Assess for malaria.
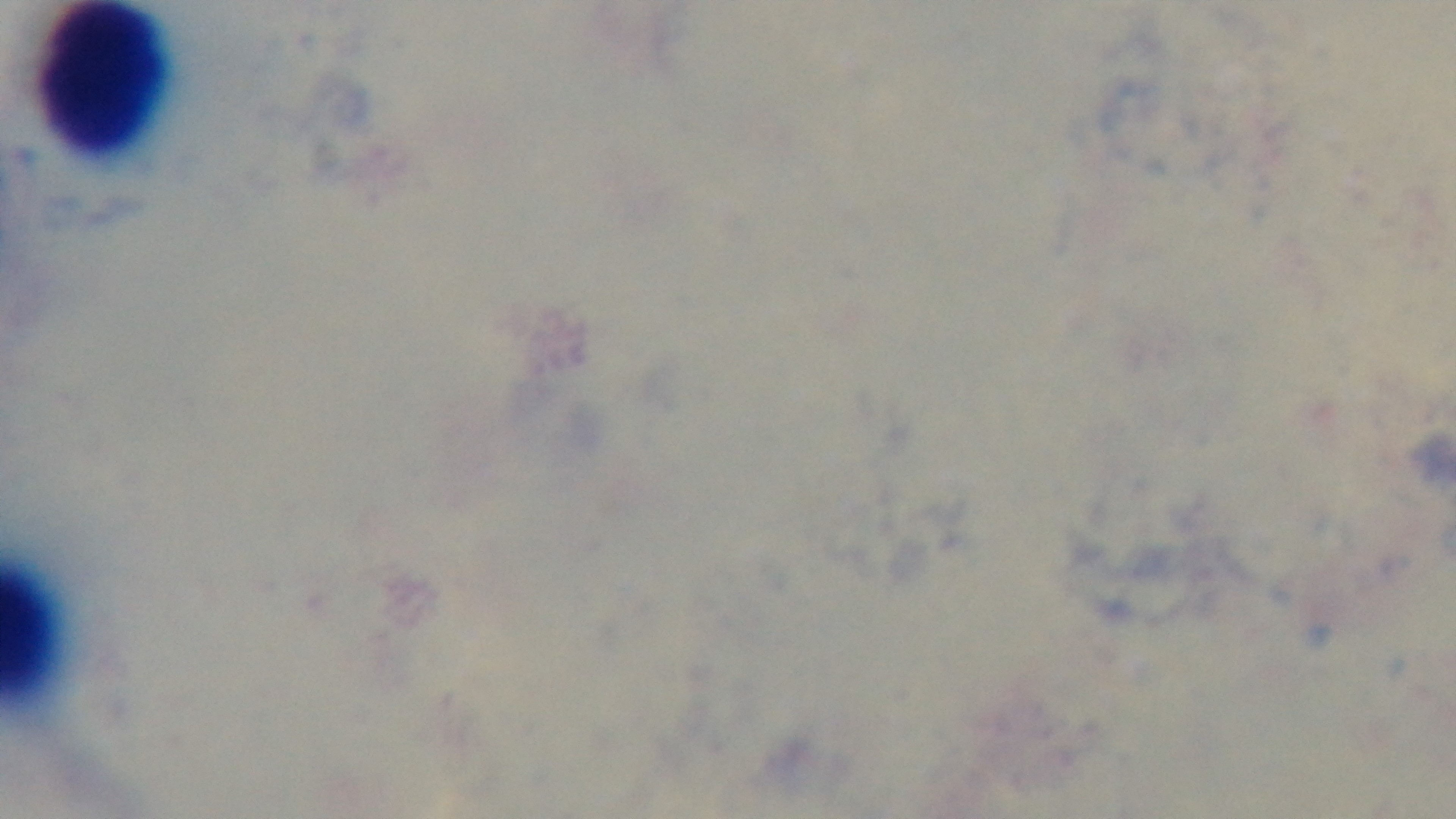
It is uninfected.

objective = 100x oil immersion
capture = mounted 4K digital camera
modality = light microscopy
preparation = thick blood film
stain = Giemsa
field of view = one from the slide